Identify the preparation type.
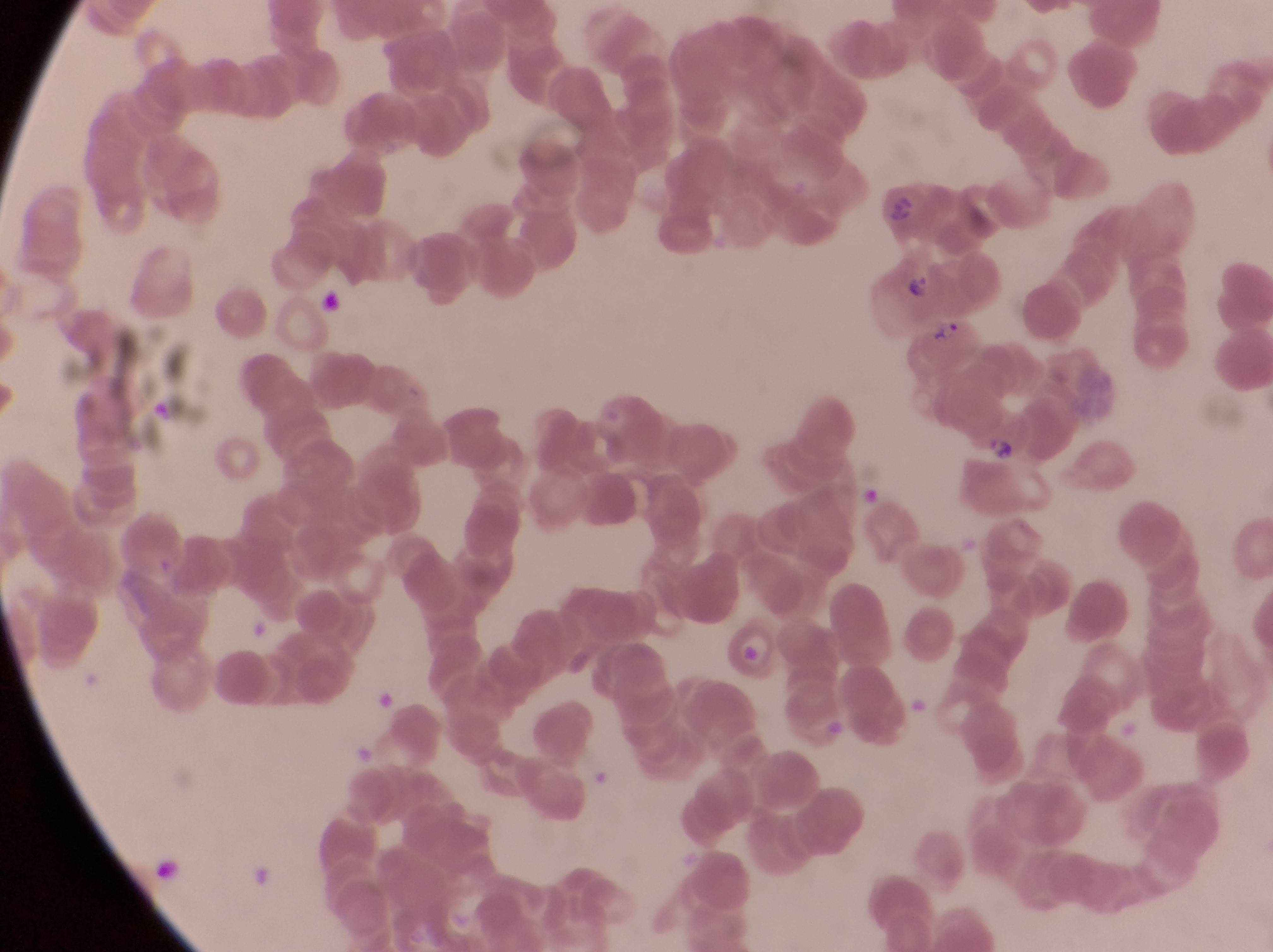
Thin blood smear.

Approximate bounding boxes as {left, top, right, bottom} in pixels.
Summary:
  - Parasitised red blood cell locations: {871, 257, 948, 332}, {903, 317, 985, 384}, {722, 624, 779, 691}
  - Trophozoite locations: {984, 434, 1017, 467}
  - Artifact (platelet-like body, stain precipitate, or debris) locations: {314, 278, 354, 333}
  - Capture: smartphone photograph through the eyepiece of an Olympus CX-23 microscope
  - Image size: 1273×952 pixels
  - Magnification: 1000x
  - Field of view: single
  - Country: Uganda